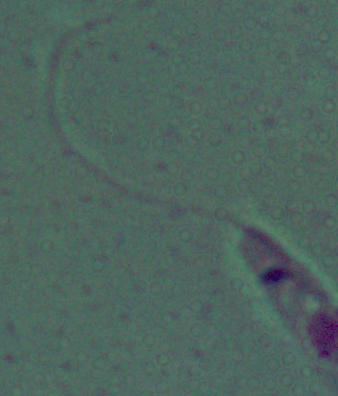
Summary:
  - Magnification: 1000x
  - Modality: micrograph
  - Identification: Leishmania